Classify this cell by malaria status.
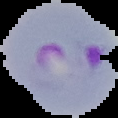

Parasitized.

{
  "preparation": "thin blood smear",
  "image_type": "cell region segmented out of the field of view; surrounding area masked to black",
  "image_size": "118×118 pixels"
}